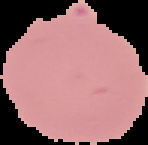

preparation = thin blood film
image size = 148×145 pixels
image type = segmented cell region with the area outside set to black
result = no Plasmodium parasites seen